Classify this cell by malaria status.
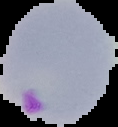

Parasitized.

From a thin blood smear. Segmented cell region on a black background. Image is 118×127 pixels.